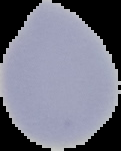

{
  "image_type": "cell region segmented out of the field of view; surrounding area masked to black",
  "preparation": "thin blood smear",
  "image_size": "121×151 pixels",
  "malaria_status": "uninfected"
}